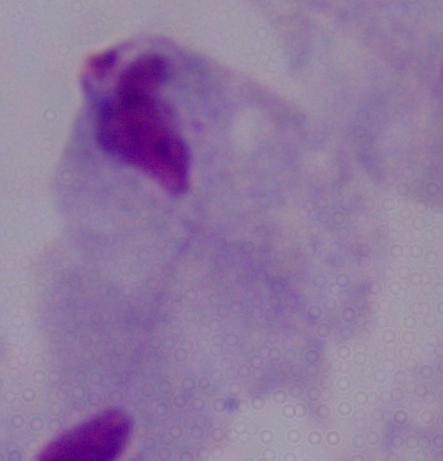
Captured at 1000x magnification. A trichomonad is seen. Photomicrograph.